Describe the morphology of the red blood cells.
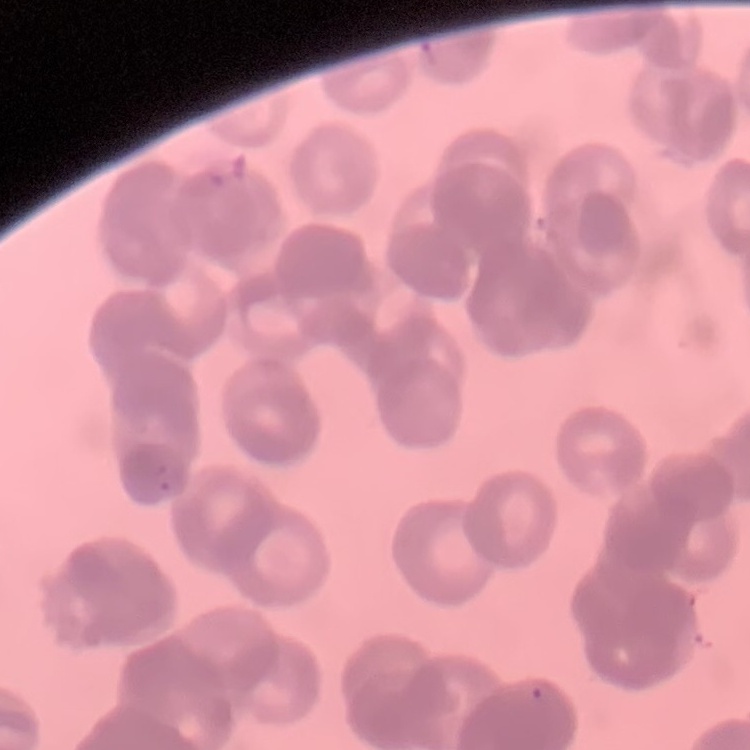
They show rouleaux formation.

One tile cut from a larger photomicrograph. Stained with either Field's or Giemsa. Thin blood film.